Give a bounding box for every Plasmodium parasite.
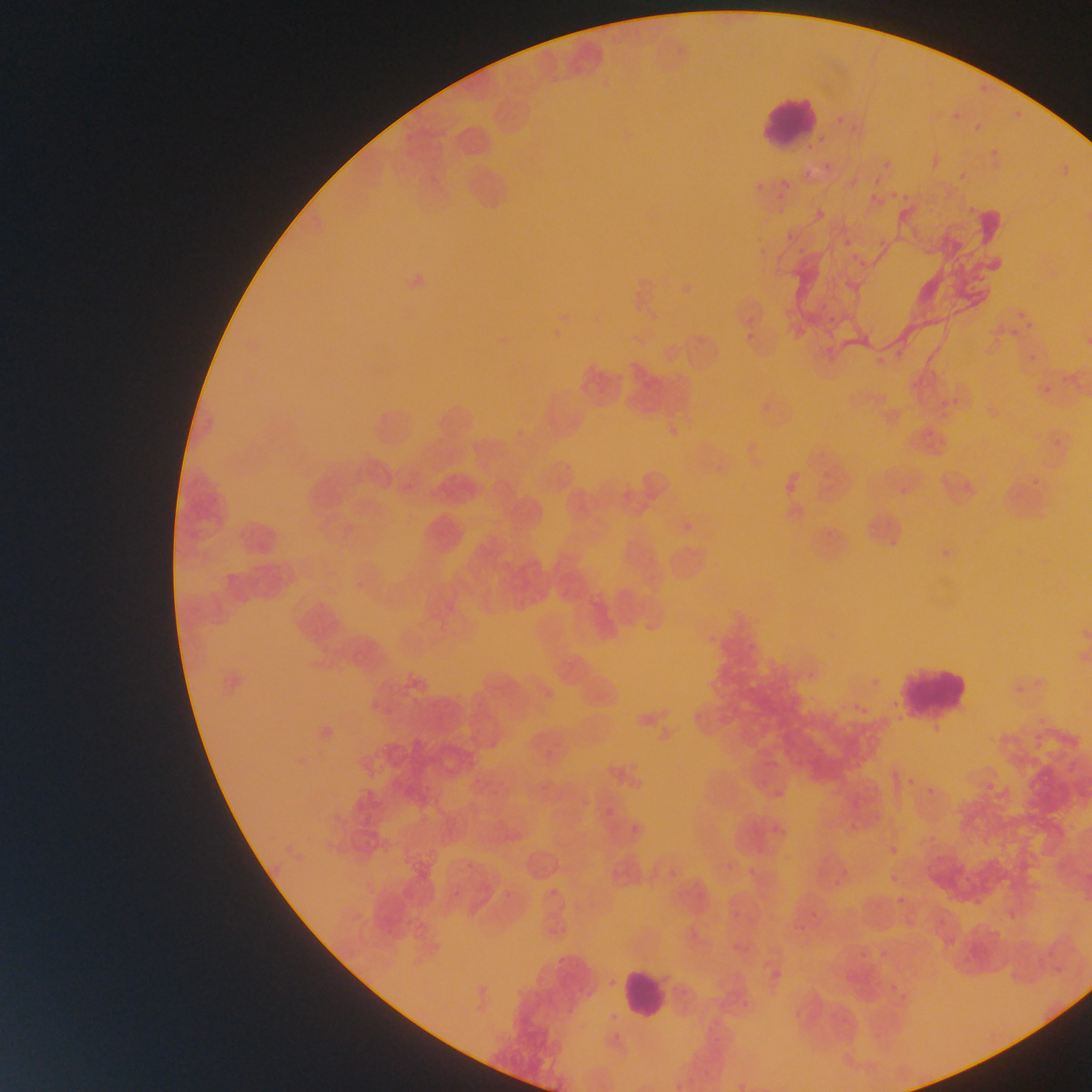
Approximate bounding boxes as (left, top, right, bottom) in pixels.
Plasmodium parasites: (977, 85, 989, 94), (1011, 109, 1022, 123), (846, 112, 874, 135), (947, 114, 959, 123), (835, 116, 849, 130), (971, 117, 986, 131), (881, 148, 895, 174), (988, 148, 1003, 157), (822, 158, 839, 170), (956, 169, 968, 183), (778, 174, 790, 188), (752, 179, 761, 192), (864, 181, 891, 203), (900, 189, 918, 203), (887, 190, 900, 199), (964, 197, 982, 214), (815, 198, 840, 215), (776, 202, 786, 215), (872, 224, 895, 248), (780, 230, 795, 239), (841, 234, 856, 251), (856, 257, 867, 265), (816, 297, 830, 312), (1010, 302, 1035, 334), (749, 316, 760, 323), (821, 318, 833, 326), (1005, 328, 1012, 340), (744, 332, 756, 345), (895, 346, 906, 360), (1026, 349, 1044, 363), (874, 352, 887, 365), (1061, 372, 1079, 383), (1039, 382, 1057, 396), (947, 390, 966, 410), (667, 427, 677, 440), (1048, 439, 1070, 451), (1030, 469, 1057, 491), (962, 470, 981, 494), (895, 484, 908, 498), (783, 485, 797, 497), (680, 517, 695, 536), (938, 542, 950, 561), (354, 579, 369, 591), (748, 633, 760, 651), (1013, 663, 1035, 702), (870, 677, 882, 689), (856, 698, 872, 715), (1034, 706, 1051, 730), (606, 808, 613, 817), (550, 889, 558, 897).

Summary:
  - Leukocyte locations: (753, 92, 822, 150), (890, 662, 973, 718), (619, 965, 668, 1021)
  - Field of view: single
  - Image size: 1092×1092 pixels
  - Country: Ghana
  - Preparation: thin blood film
  - Capture: mobile-phone photograph through a microscope